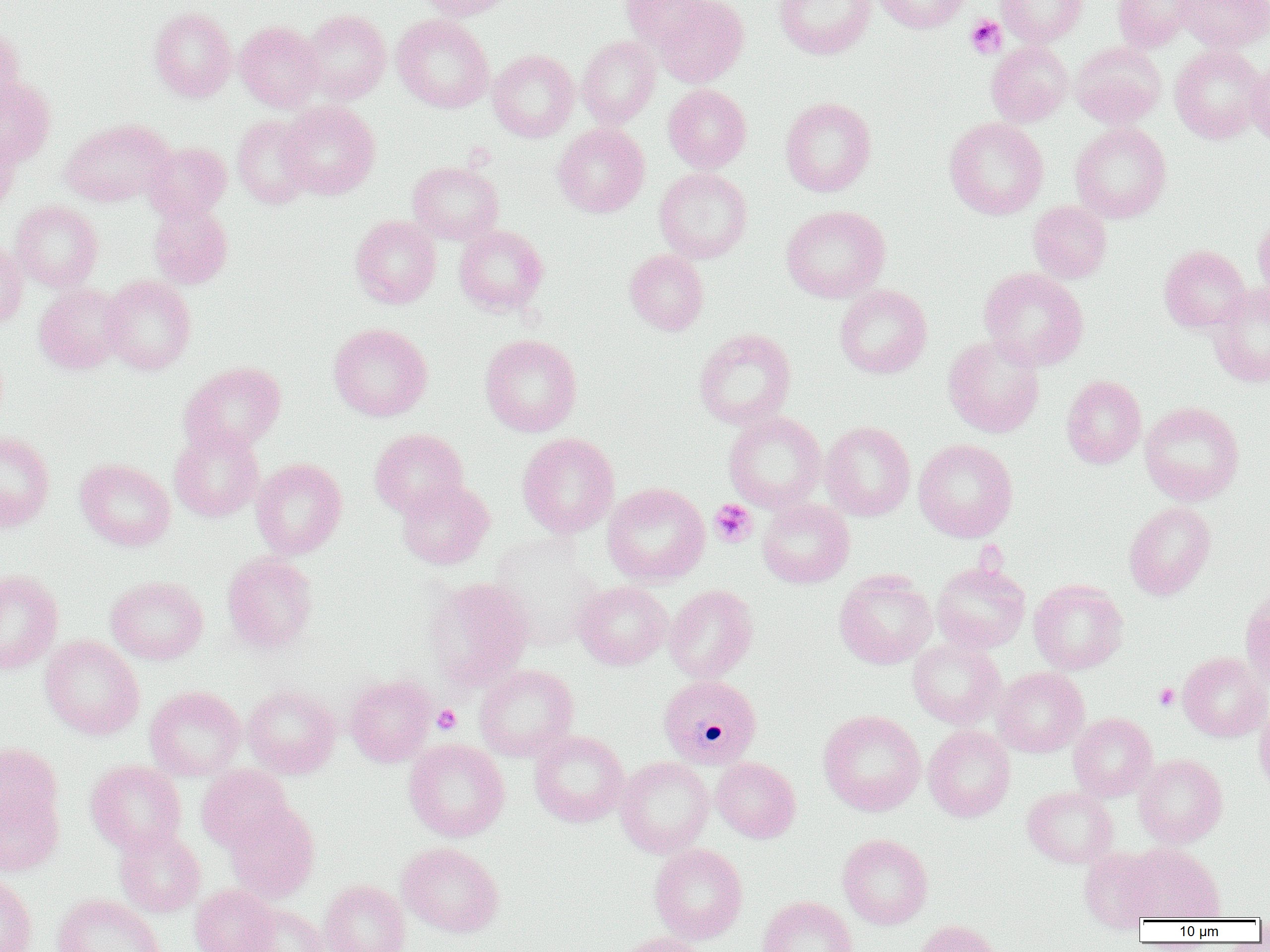
Summary:
  - Coordinate format: approximate bounding boxes as [x1, y1, x2, y2] in pixels
  - Uninfected red blood cell locations: [417, 0, 513, 21], [621, 0, 712, 52], [652, 0, 749, 87], [774, 0, 875, 60], [874, 0, 970, 34], [996, 0, 1088, 46], [1112, 0, 1199, 52], [1173, 0, 1270, 52], [149, 7, 236, 102], [300, 9, 391, 103], [295, 11, 385, 197], [392, 14, 493, 113], [235, 21, 324, 111], [0, 25, 25, 116], [577, 36, 661, 128], [987, 40, 1073, 127], [1070, 42, 1167, 129], [1169, 44, 1268, 144], [487, 49, 579, 142], [1247, 59, 1270, 146], [0, 79, 55, 167], [663, 84, 751, 173], [780, 97, 877, 197], [280, 101, 380, 199], [232, 115, 316, 208], [944, 117, 1048, 219], [60, 118, 174, 206], [553, 123, 649, 217], [1070, 123, 1171, 223], [0, 133, 20, 219], [143, 135, 315, 215], [143, 142, 231, 222], [408, 161, 503, 244], [654, 167, 753, 263], [10, 200, 103, 292], [1027, 201, 1112, 283], [148, 202, 233, 289], [781, 205, 890, 303], [1253, 213, 1270, 305], [351, 215, 441, 308], [454, 225, 549, 315], [0, 239, 27, 328], [1159, 245, 1250, 333], [625, 249, 709, 335], [979, 267, 1088, 370], [101, 276, 196, 374], [34, 284, 126, 374], [834, 284, 932, 378], [1208, 284, 1270, 387], [328, 323, 432, 421], [694, 328, 796, 430], [480, 334, 581, 436], [943, 335, 1044, 438], [180, 361, 285, 456], [1061, 375, 1146, 469], [1140, 401, 1244, 505], [723, 411, 826, 513], [820, 421, 915, 521], [169, 428, 264, 522], [370, 428, 468, 518], [0, 432, 54, 531], [517, 433, 619, 538], [913, 439, 1018, 542], [75, 458, 175, 551], [251, 458, 346, 558], [396, 479, 494, 569], [603, 483, 710, 585], [757, 499, 854, 588], [1123, 502, 1216, 600], [489, 536, 603, 651], [222, 552, 317, 654], [931, 562, 1030, 653], [0, 569, 63, 674], [834, 570, 937, 669], [106, 576, 208, 665], [425, 577, 532, 690], [1028, 579, 1128, 674], [574, 581, 672, 670], [1240, 583, 1270, 692], [664, 585, 759, 683], [40, 635, 144, 740], [907, 638, 1006, 729], [1177, 652, 1270, 741], [474, 664, 578, 761], [993, 667, 1089, 757], [344, 675, 436, 767], [243, 684, 341, 778], [145, 686, 246, 781], [1254, 700, 1270, 799], [819, 710, 925, 816], [1069, 712, 1157, 801], [923, 725, 1015, 822], [529, 730, 629, 827], [404, 739, 509, 841], [1, 743, 61, 836], [1134, 754, 1228, 847], [615, 756, 714, 857], [711, 757, 800, 842], [85, 760, 186, 854], [196, 764, 293, 853], [1022, 786, 1119, 868], [0, 790, 64, 876], [225, 802, 319, 903], [114, 827, 205, 917], [837, 834, 933, 929], [398, 842, 503, 938], [1124, 842, 1224, 922], [649, 843, 747, 943], [1079, 847, 1161, 932], [0, 873, 36, 952], [319, 880, 410, 952], [190, 885, 280, 952], [52, 894, 164, 952], [757, 896, 857, 952], [241, 903, 328, 952], [913, 920, 1002, 952], [613, 932, 710, 952]
  - Platelet locations: [966, 15, 1006, 58], [709, 499, 757, 547], [1154, 683, 1179, 709], [432, 705, 461, 733]
  - Plasmodium malariae-infected red blood cell locations: [658, 674, 762, 769]
  - Slide-level diagnosis: Plasmodium malariae
  - Magnification: 1000x
  - Image size: 1270×952 pixels
  - Preparation: thin blood smear
  - Field of view: one of a larger specimen
  - Modality: light microscopy